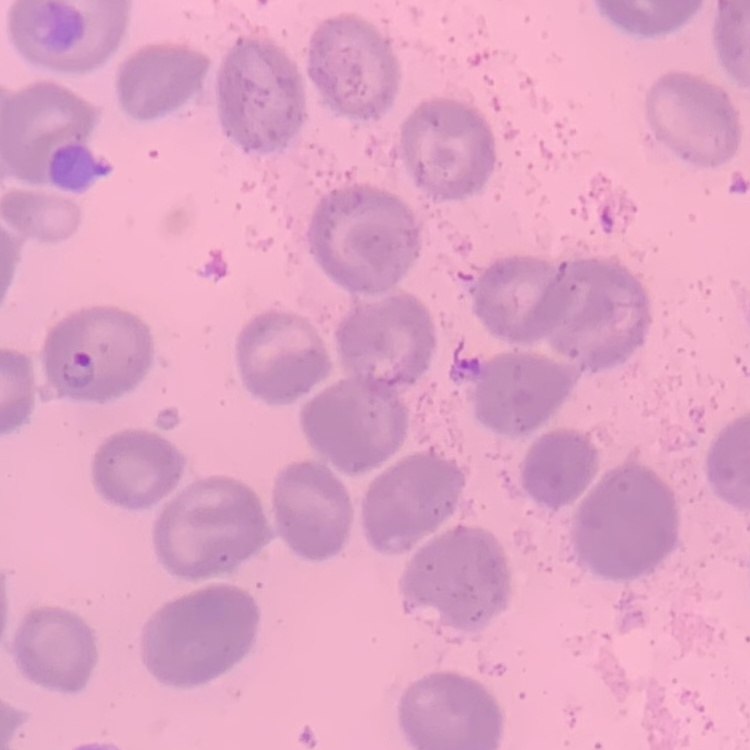

The erythrocytes exhibit no rouleaux formation. Thin blood film. Square crop of a larger photomicrograph. Stained with either Field's or Giemsa.